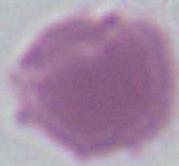

Summary:
  - Magnification: 1000x
  - Identification: red blood cell
  - Modality: micrograph